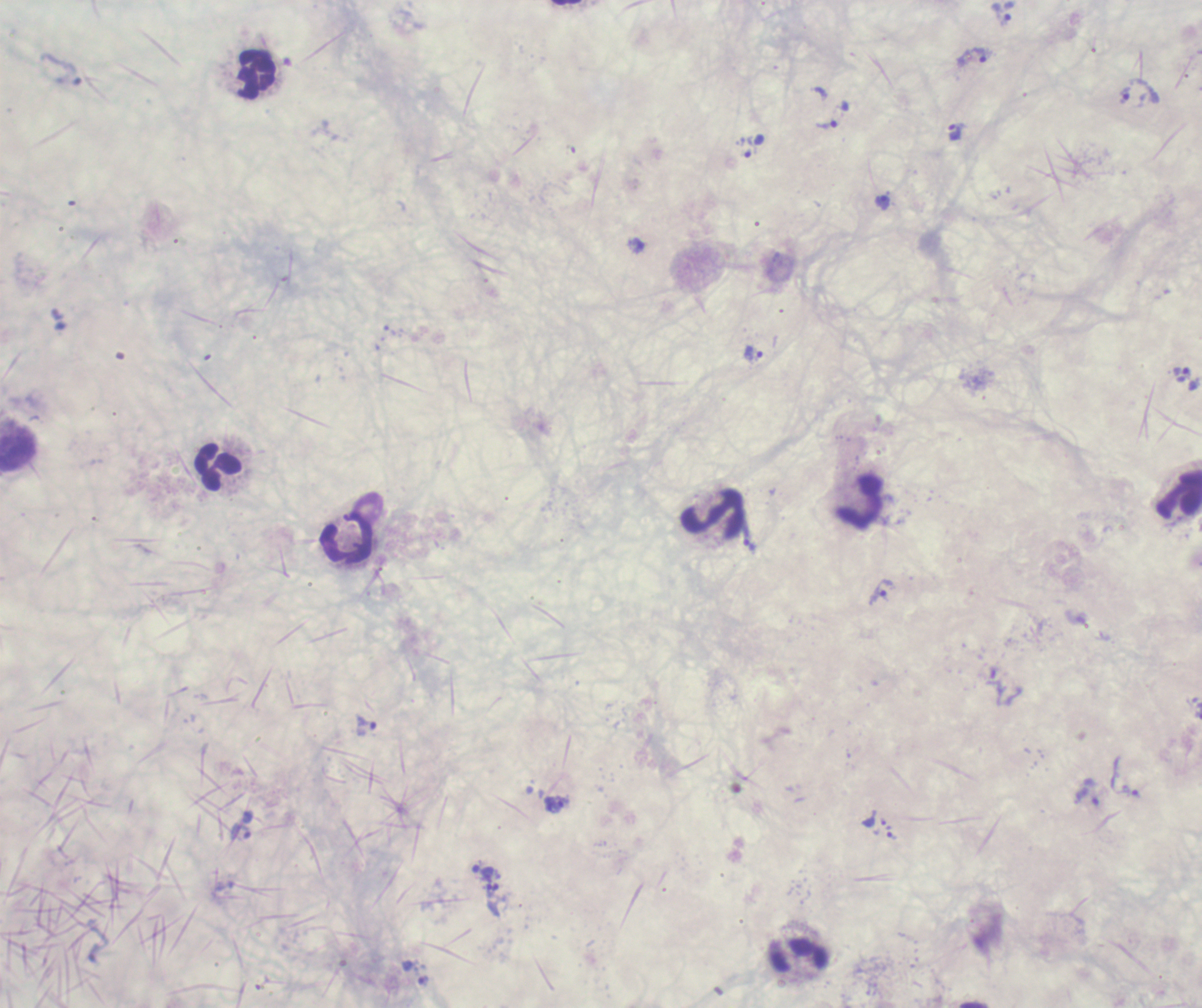
Approximate centers as [x, y] in pixels.
Summary:
  - Leukocyte locations: [257, 74], [218, 466], [1179, 492], [860, 502], [714, 513], [347, 539], [800, 953]
  - Trophozoite locations: [1003, 20], [974, 54], [1125, 95], [826, 125], [955, 133], [883, 202], [754, 353], [1181, 374], [750, 545], [881, 591], [996, 681], [366, 726], [1128, 791], [1088, 792], [556, 804], [240, 831], [891, 836], [498, 893]
  - Magnification: 100x
  - Image size: 1202×1008 pixels
  - Preparation: thick blood smear
  - Result: Plasmodium parasites identified
  - Context: previously used in a real diagnosis
  - Field of view: one from this slide
  - Stain: Romanowsky
  - Background quality: poor
  - Coloration quality: bad